Assess this cell for malaria.
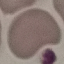

Uninfected.

stain = Giemsa
capture = smartphone through the microscope eyepiece
preparation = thin blood film
image type = cell patch, automatically extracted from a larger field of view and resized to 64 × 64 pixels